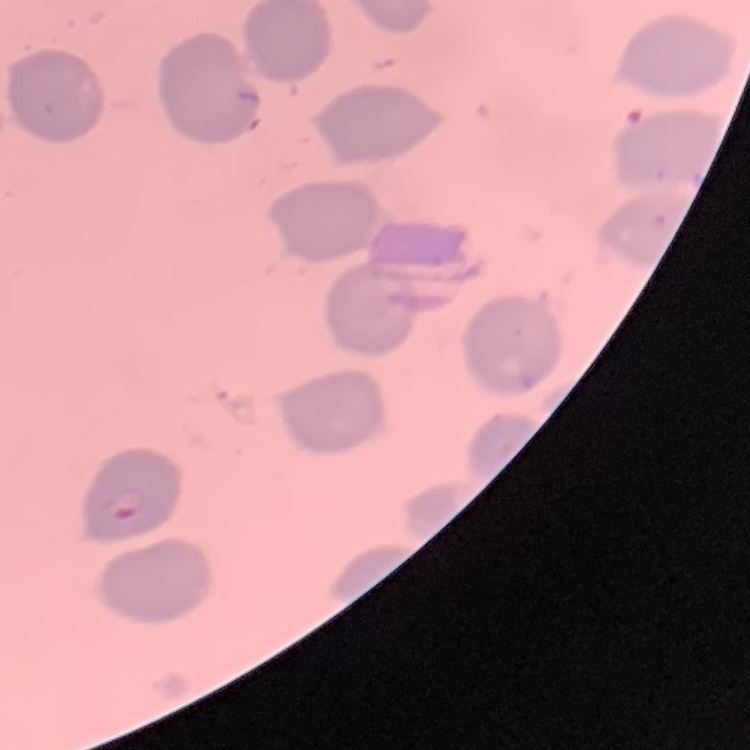

Summary:
  - Red blood cell morphology: no rouleaux formation
  - Stain: Field's or Giemsa
  - Preparation: thin peripheral smear
  - Image type: square crop of a larger photomicrograph